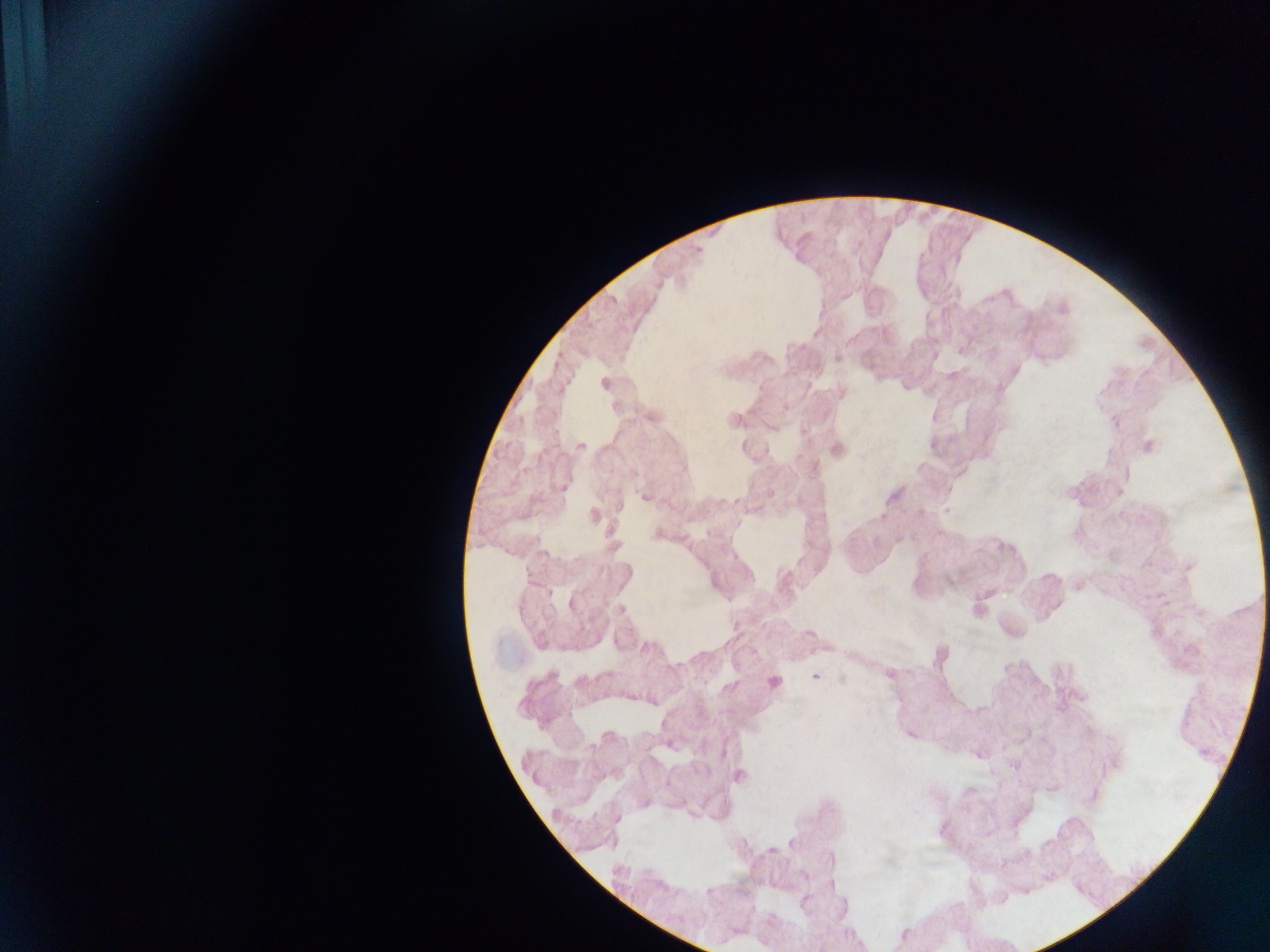

Approximate centers as (x, y) in pixels.
Summary:
  - Plasmodium parasite locations: (947, 512), (815, 678)
  - Leukocyte locations: (836, 448), (772, 682)
  - Field of view: single
  - Capture: mobile-phone photograph through a microscope
  - Country: Ghana
  - Preparation: thick blood smear
  - Image size: 1270×952 pixels